Identify the parasite.
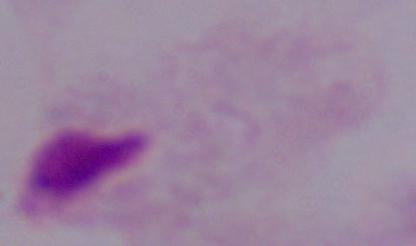

This is a trichomonad.

Micrograph. Captured at 1000x magnification.